Name the blood parasite species.
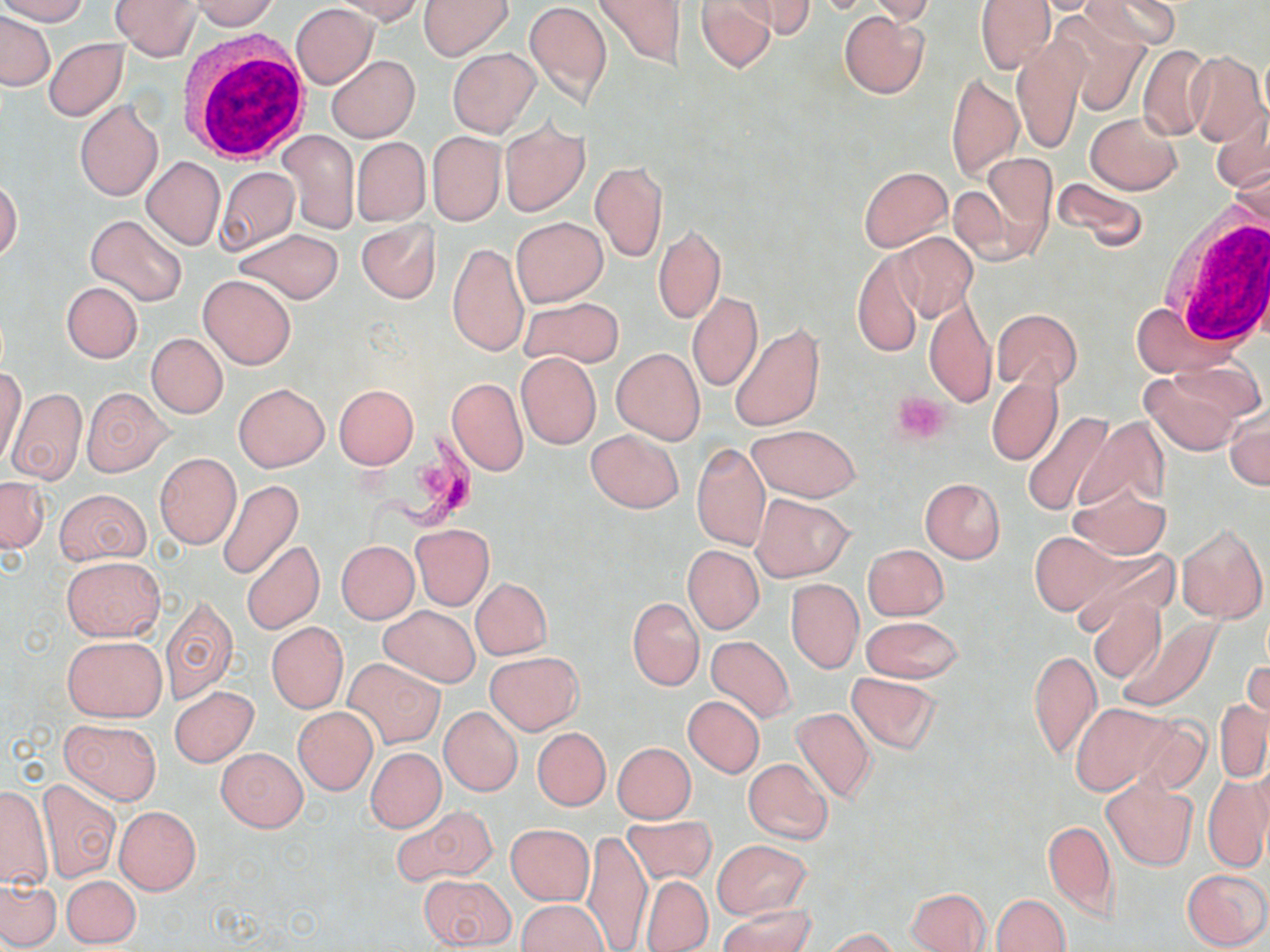

Trypanosoma brucei.

Approximate bounding boxes as named x1/y1/x2/y2 corners in pixels. Trypanosoma brucei locations: (x1=357, y1=435, x2=489, y2=556). Uninfected red blood cell locations: (x1=0, y1=0, x2=89, y2=25), (x1=111, y1=0, x2=202, y2=60), (x1=190, y1=0, x2=280, y2=31), (x1=329, y1=0, x2=423, y2=22), (x1=419, y1=0, x2=512, y2=60), (x1=524, y1=0, x2=612, y2=110), (x1=591, y1=0, x2=686, y2=69), (x1=738, y1=0, x2=815, y2=39), (x1=976, y1=0, x2=1055, y2=74), (x1=1030, y1=0, x2=1113, y2=14), (x1=1085, y1=0, x2=1181, y2=53), (x1=694, y1=1, x2=776, y2=73), (x1=869, y1=1, x2=933, y2=24), (x1=291, y1=4, x2=377, y2=88), (x1=839, y1=9, x2=928, y2=99), (x1=1050, y1=9, x2=1152, y2=114), (x1=1, y1=12, x2=55, y2=90), (x1=44, y1=38, x2=128, y2=121), (x1=1013, y1=39, x2=1084, y2=154), (x1=1137, y1=45, x2=1211, y2=141), (x1=448, y1=49, x2=540, y2=137), (x1=1186, y1=50, x2=1268, y2=148), (x1=327, y1=55, x2=420, y2=143), (x1=947, y1=73, x2=1022, y2=180), (x1=74, y1=99, x2=163, y2=201), (x1=1211, y1=110, x2=1270, y2=197), (x1=1085, y1=112, x2=1181, y2=194), (x1=499, y1=119, x2=589, y2=218), (x1=280, y1=131, x2=359, y2=234), (x1=426, y1=131, x2=505, y2=226), (x1=352, y1=137, x2=429, y2=225), (x1=979, y1=152, x2=1055, y2=244), (x1=140, y1=156, x2=225, y2=250), (x1=590, y1=160, x2=668, y2=263), (x1=1228, y1=163, x2=1270, y2=240), (x1=216, y1=166, x2=298, y2=253), (x1=859, y1=166, x2=952, y2=251), (x1=1052, y1=175, x2=1148, y2=252), (x1=0, y1=178, x2=22, y2=261), (x1=86, y1=214, x2=187, y2=307), (x1=512, y1=216, x2=606, y2=306), (x1=357, y1=219, x2=441, y2=303), (x1=653, y1=223, x2=725, y2=322), (x1=235, y1=228, x2=343, y2=304), (x1=892, y1=232, x2=977, y2=323), (x1=448, y1=242, x2=528, y2=357), (x1=854, y1=251, x2=925, y2=358), (x1=199, y1=275, x2=296, y2=369), (x1=61, y1=281, x2=141, y2=363), (x1=687, y1=292, x2=763, y2=393), (x1=923, y1=293, x2=996, y2=411), (x1=520, y1=295, x2=621, y2=368), (x1=1131, y1=302, x2=1229, y2=378), (x1=992, y1=309, x2=1082, y2=390), (x1=730, y1=324, x2=823, y2=431), (x1=147, y1=333, x2=227, y2=418), (x1=611, y1=347, x2=705, y2=444), (x1=516, y1=352, x2=600, y2=448), (x1=1, y1=368, x2=26, y2=468), (x1=1139, y1=369, x2=1250, y2=455), (x1=986, y1=375, x2=1062, y2=466), (x1=446, y1=377, x2=528, y2=476), (x1=234, y1=383, x2=328, y2=471), (x1=334, y1=384, x2=418, y2=468), (x1=5, y1=388, x2=86, y2=485), (x1=82, y1=388, x2=171, y2=476), (x1=1225, y1=406, x2=1269, y2=490), (x1=1022, y1=411, x2=1116, y2=515), (x1=1079, y1=415, x2=1168, y2=515), (x1=748, y1=425, x2=860, y2=501), (x1=585, y1=429, x2=684, y2=514), (x1=691, y1=443, x2=770, y2=552), (x1=155, y1=452, x2=240, y2=549), (x1=0, y1=477, x2=48, y2=553), (x1=920, y1=477, x2=1005, y2=562), (x1=217, y1=480, x2=303, y2=581), (x1=1069, y1=481, x2=1170, y2=561), (x1=55, y1=488, x2=150, y2=565), (x1=751, y1=494, x2=854, y2=580), (x1=1177, y1=523, x2=1267, y2=622), (x1=409, y1=524, x2=493, y2=609), (x1=1030, y1=533, x2=1114, y2=613), (x1=242, y1=540, x2=324, y2=635), (x1=337, y1=541, x2=419, y2=623), (x1=862, y1=544, x2=948, y2=620), (x1=683, y1=546, x2=764, y2=634), (x1=1069, y1=546, x2=1176, y2=634), (x1=62, y1=556, x2=164, y2=641), (x1=471, y1=577, x2=551, y2=660), (x1=785, y1=579, x2=863, y2=673), (x1=159, y1=593, x2=239, y2=706), (x1=1088, y1=594, x2=1166, y2=685), (x1=628, y1=597, x2=703, y2=691), (x1=379, y1=606, x2=479, y2=687), (x1=860, y1=615, x2=963, y2=684), (x1=1117, y1=617, x2=1221, y2=712), (x1=267, y1=622, x2=348, y2=713), (x1=61, y1=635, x2=166, y2=721), (x1=706, y1=635, x2=794, y2=722), (x1=1029, y1=648, x2=1101, y2=762), (x1=485, y1=651, x2=584, y2=734), (x1=1243, y1=657, x2=1269, y2=724), (x1=343, y1=658, x2=444, y2=748), (x1=847, y1=672, x2=941, y2=754), (x1=170, y1=686, x2=258, y2=767), (x1=683, y1=694, x2=765, y2=778), (x1=1216, y1=699, x2=1269, y2=783), (x1=1071, y1=703, x2=1173, y2=794), (x1=791, y1=705, x2=877, y2=804), (x1=293, y1=706, x2=377, y2=794), (x1=440, y1=707, x2=523, y2=796), (x1=1130, y1=716, x2=1213, y2=797), (x1=60, y1=719, x2=160, y2=803), (x1=533, y1=727, x2=611, y2=810), (x1=613, y1=742, x2=695, y2=823), (x1=216, y1=747, x2=307, y2=831), (x1=366, y1=747, x2=446, y2=832), (x1=743, y1=757, x2=834, y2=844), (x1=1250, y1=768, x2=1270, y2=863), (x1=1204, y1=775, x2=1269, y2=873), (x1=37, y1=779, x2=120, y2=883), (x1=1102, y1=779, x2=1199, y2=870), (x1=0, y1=785, x2=53, y2=887), (x1=392, y1=805, x2=497, y2=887), (x1=114, y1=806, x2=201, y2=895), (x1=623, y1=815, x2=717, y2=885), (x1=1044, y1=820, x2=1118, y2=921), (x1=505, y1=823, x2=594, y2=905), (x1=582, y1=831, x2=652, y2=951), (x1=711, y1=838, x2=812, y2=919), (x1=1182, y1=867, x2=1269, y2=950), (x1=417, y1=874, x2=515, y2=949), (x1=62, y1=875, x2=140, y2=948), (x1=640, y1=876, x2=712, y2=951), (x1=0, y1=880, x2=61, y2=949), (x1=906, y1=887, x2=993, y2=951), (x1=993, y1=893, x2=1069, y2=952), (x1=518, y1=900, x2=608, y2=952), (x1=718, y1=905, x2=815, y2=952), (x1=823, y1=928, x2=900, y2=952). Platelet locations: (x1=892, y1=391, x2=950, y2=444). White blood cell locations: (x1=179, y1=33, x2=311, y2=161), (x1=1158, y1=214, x2=1270, y2=347). Light microscopy. Captured at 1000x magnification. One field of a larger specimen. Thin blood smear. May-Grünwald-Giemsa stain. Image is 1270×952 pixels.